Classify this cell by malaria status.
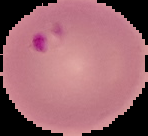

Parasitized.

Summary:
  - Image size: 148×136 pixels
  - Image type: segmented cell region with the area outside set to black
  - Preparation: thin blood film